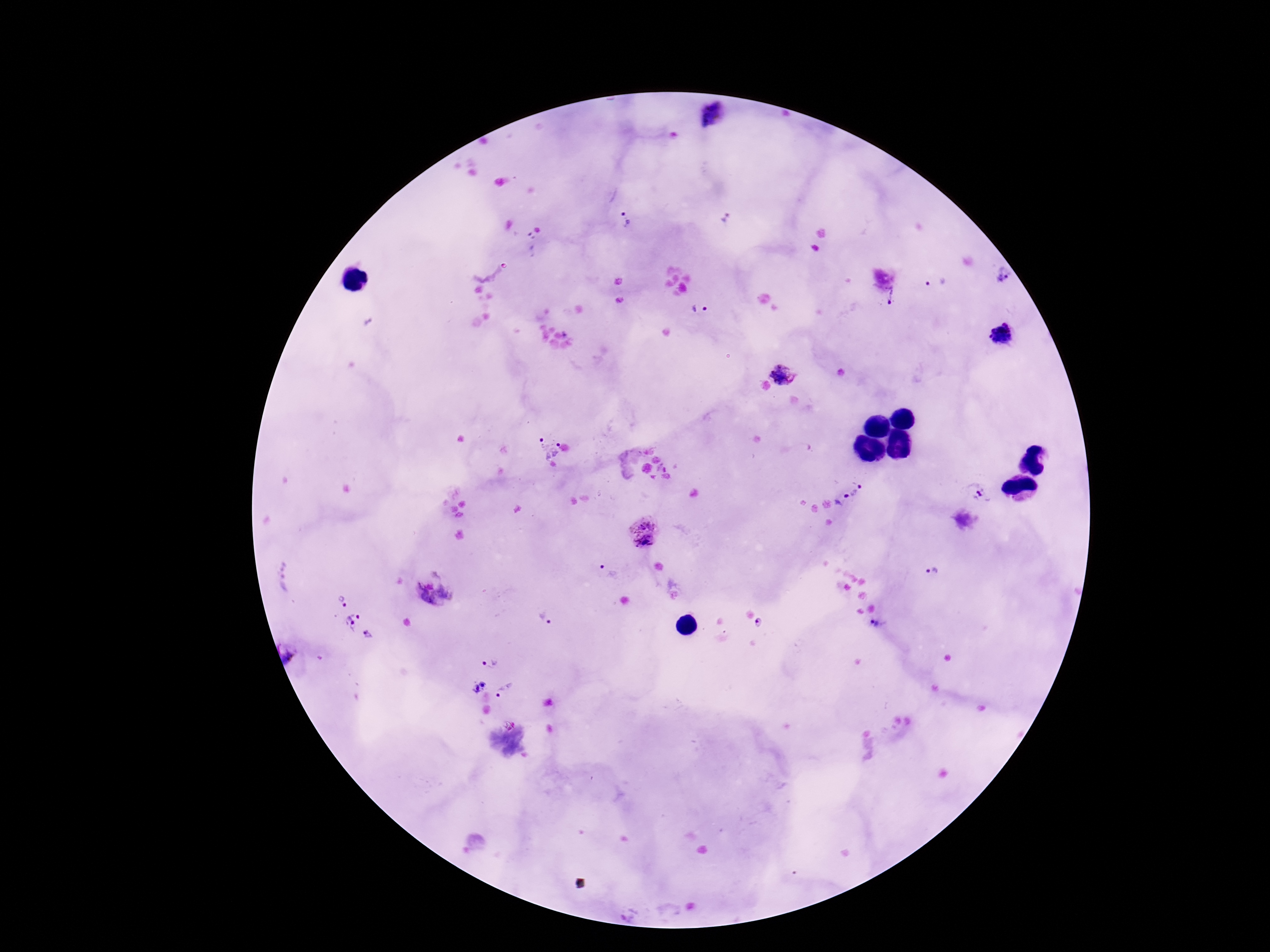

capture: smartphone camera through the microscope eyepiece
patient_malaria_status: positive
field_of_view: single
magnification: 100x
preparation: thick blood film
image_size: 1270×952 pixels
stain: Giemsa
plasmodium_parasite_locations: 'approximate object centers, in pixels from the top-left corner: (x=711, y=114), (x=727, y=217), (x=625, y=220), (x=1004, y=277), (x=932, y=281), (x=891, y=297), (x=703, y=312), (x=1004, y=334), (x=785, y=369), (x=547, y=446), (x=860, y=487), (x=854, y=493), (x=978, y=493), (x=847, y=496), (x=838, y=503), (x=644, y=532), (x=603, y=566), (x=933, y=573), (x=435, y=591), (x=342, y=600), (x=544, y=619), (x=351, y=620), (x=759, y=622), (x=876, y=625), (x=369, y=633), (x=292, y=653), (x=489, y=664), (x=478, y=687), (x=505, y=691), (x=509, y=724)'